Identify the cell.
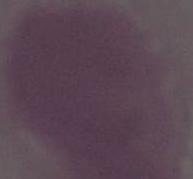
This is an erythrocyte.

1000x magnification. Micrograph.